Name the cell type shown.
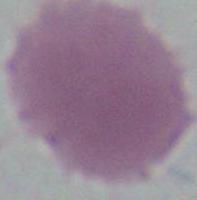
This is an erythrocyte.

{
  "modality": "micrograph",
  "magnification": "1000x"
}